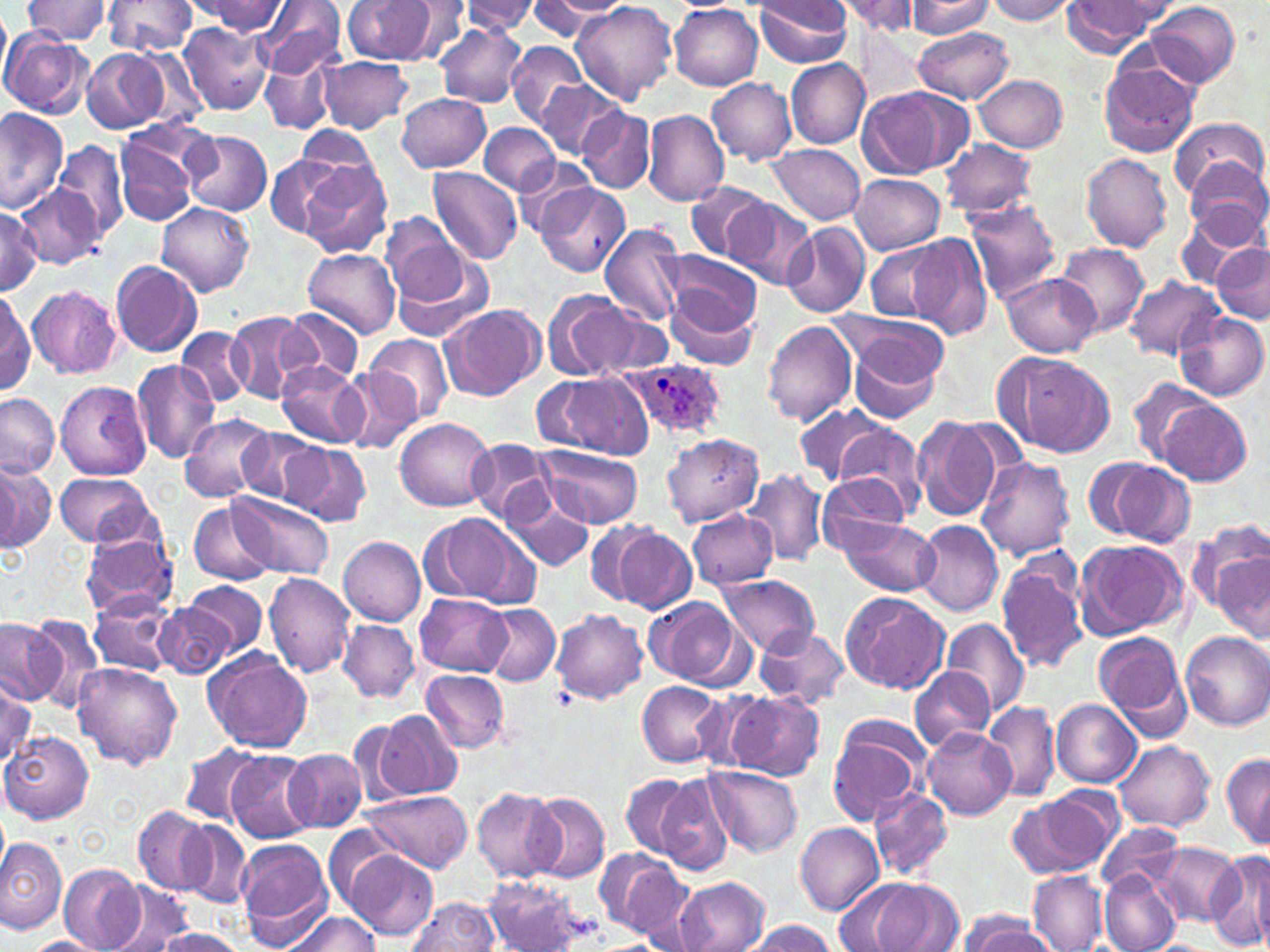

Summary:
  - Coordinate format: approximate bounding boxes as named x1/y1/x2/y2 corners in pixels
  - Plasmodium ovale-infected red blood cell locations: (x1=623, y1=358, x2=727, y2=441)
  - Uninfected red blood cell locations: (x1=23, y1=0, x2=113, y2=44), (x1=102, y1=0, x2=197, y2=57), (x1=256, y1=0, x2=345, y2=81), (x1=343, y1=0, x2=437, y2=64), (x1=752, y1=0, x2=854, y2=67), (x1=985, y1=0, x2=1077, y2=23), (x1=192, y1=1, x2=287, y2=35), (x1=402, y1=1, x2=472, y2=61), (x1=460, y1=1, x2=541, y2=34), (x1=538, y1=1, x2=629, y2=22), (x1=835, y1=1, x2=925, y2=35), (x1=905, y1=1, x2=996, y2=37), (x1=1061, y1=1, x2=1175, y2=54), (x1=529, y1=2, x2=616, y2=39), (x1=569, y1=2, x2=678, y2=107), (x1=1147, y1=2, x2=1241, y2=86), (x1=0, y1=6, x2=13, y2=89), (x1=670, y1=6, x2=763, y2=89), (x1=178, y1=23, x2=274, y2=115), (x1=435, y1=23, x2=526, y2=107), (x1=910, y1=27, x2=1015, y2=104), (x1=0, y1=31, x2=92, y2=118), (x1=506, y1=39, x2=587, y2=130), (x1=81, y1=47, x2=169, y2=132), (x1=260, y1=52, x2=339, y2=135), (x1=317, y1=56, x2=413, y2=134), (x1=1098, y1=56, x2=1200, y2=159), (x1=786, y1=57, x2=871, y2=149), (x1=776, y1=61, x2=879, y2=225), (x1=975, y1=75, x2=1069, y2=152), (x1=535, y1=78, x2=626, y2=160), (x1=707, y1=78, x2=797, y2=164), (x1=858, y1=87, x2=963, y2=178), (x1=398, y1=92, x2=491, y2=173), (x1=577, y1=107, x2=655, y2=193), (x1=0, y1=110, x2=68, y2=213), (x1=643, y1=110, x2=730, y2=207), (x1=1170, y1=117, x2=1266, y2=202), (x1=479, y1=121, x2=561, y2=196), (x1=294, y1=128, x2=383, y2=208), (x1=182, y1=130, x2=273, y2=215), (x1=940, y1=138, x2=1037, y2=220), (x1=113, y1=139, x2=197, y2=228), (x1=54, y1=140, x2=128, y2=239), (x1=766, y1=145, x2=865, y2=225), (x1=1080, y1=152, x2=1174, y2=251), (x1=264, y1=153, x2=349, y2=240), (x1=513, y1=155, x2=597, y2=237), (x1=1186, y1=157, x2=1269, y2=246), (x1=299, y1=161, x2=394, y2=260), (x1=427, y1=166, x2=523, y2=265), (x1=850, y1=176, x2=944, y2=254), (x1=534, y1=181, x2=629, y2=277), (x1=686, y1=182, x2=770, y2=260), (x1=20, y1=188, x2=99, y2=270), (x1=722, y1=196, x2=817, y2=289), (x1=962, y1=198, x2=1061, y2=302), (x1=156, y1=201, x2=255, y2=297), (x1=0, y1=204, x2=43, y2=293), (x1=1175, y1=204, x2=1265, y2=287), (x1=381, y1=214, x2=470, y2=307), (x1=599, y1=222, x2=688, y2=329), (x1=781, y1=222, x2=871, y2=319), (x1=906, y1=232, x2=993, y2=339), (x1=863, y1=241, x2=955, y2=323), (x1=1210, y1=242, x2=1270, y2=322), (x1=1057, y1=243, x2=1150, y2=336), (x1=389, y1=247, x2=496, y2=343), (x1=302, y1=248, x2=400, y2=339), (x1=667, y1=251, x2=764, y2=332), (x1=110, y1=260, x2=202, y2=357), (x1=999, y1=273, x2=1100, y2=356), (x1=1124, y1=274, x2=1223, y2=358), (x1=27, y1=284, x2=122, y2=378), (x1=663, y1=288, x2=759, y2=371), (x1=1, y1=290, x2=35, y2=393), (x1=542, y1=290, x2=638, y2=383), (x1=440, y1=304, x2=544, y2=400), (x1=585, y1=305, x2=676, y2=380), (x1=283, y1=308, x2=363, y2=386), (x1=225, y1=311, x2=315, y2=403), (x1=1173, y1=311, x2=1267, y2=402), (x1=838, y1=314, x2=949, y2=417), (x1=762, y1=319, x2=858, y2=427), (x1=175, y1=327, x2=254, y2=407), (x1=364, y1=333, x2=453, y2=424), (x1=999, y1=350, x2=1115, y2=458), (x1=131, y1=360, x2=222, y2=464), (x1=277, y1=360, x2=369, y2=450), (x1=340, y1=371, x2=422, y2=451), (x1=541, y1=373, x2=653, y2=459), (x1=55, y1=380, x2=150, y2=480), (x1=1128, y1=380, x2=1219, y2=466), (x1=0, y1=393, x2=59, y2=479), (x1=1157, y1=399, x2=1252, y2=485), (x1=795, y1=403, x2=891, y2=487), (x1=180, y1=412, x2=275, y2=502), (x1=910, y1=415, x2=1004, y2=524), (x1=395, y1=417, x2=495, y2=512), (x1=834, y1=425, x2=929, y2=520), (x1=235, y1=427, x2=320, y2=503), (x1=663, y1=433, x2=765, y2=525), (x1=465, y1=439, x2=555, y2=523), (x1=280, y1=442, x2=371, y2=527), (x1=537, y1=446, x2=643, y2=527), (x1=976, y1=456, x2=1076, y2=561), (x1=1083, y1=457, x2=1194, y2=547), (x1=0, y1=460, x2=52, y2=552), (x1=742, y1=470, x2=829, y2=567), (x1=55, y1=474, x2=152, y2=548), (x1=818, y1=474, x2=911, y2=556), (x1=502, y1=482, x2=596, y2=574), (x1=230, y1=492, x2=333, y2=579), (x1=189, y1=500, x2=275, y2=586), (x1=688, y1=510, x2=778, y2=590), (x1=424, y1=512, x2=538, y2=611), (x1=837, y1=517, x2=939, y2=597), (x1=1186, y1=519, x2=1270, y2=617), (x1=586, y1=520, x2=666, y2=607), (x1=913, y1=520, x2=1003, y2=615), (x1=612, y1=528, x2=698, y2=613), (x1=80, y1=531, x2=180, y2=617), (x1=339, y1=537, x2=427, y2=625), (x1=1075, y1=539, x2=1187, y2=639), (x1=1212, y1=550, x2=1270, y2=638), (x1=995, y1=552, x2=1089, y2=673), (x1=264, y1=572, x2=354, y2=677), (x1=717, y1=573, x2=821, y2=656), (x1=187, y1=579, x2=268, y2=656), (x1=840, y1=590, x2=951, y2=695), (x1=90, y1=594, x2=178, y2=677), (x1=416, y1=595, x2=511, y2=676), (x1=644, y1=596, x2=746, y2=688), (x1=155, y1=600, x2=235, y2=679), (x1=478, y1=603, x2=559, y2=686), (x1=551, y1=608, x2=648, y2=704), (x1=26, y1=614, x2=107, y2=711), (x1=939, y1=616, x2=1031, y2=719), (x1=0, y1=618, x2=63, y2=704), (x1=338, y1=620, x2=418, y2=703), (x1=754, y1=625, x2=850, y2=709), (x1=1092, y1=631, x2=1191, y2=735), (x1=1181, y1=631, x2=1270, y2=730), (x1=204, y1=650, x2=314, y2=753), (x1=74, y1=664, x2=183, y2=769), (x1=911, y1=665, x2=994, y2=753), (x1=422, y1=668, x2=510, y2=753), (x1=1, y1=675, x2=36, y2=765), (x1=637, y1=681, x2=725, y2=767), (x1=724, y1=691, x2=825, y2=781), (x1=1052, y1=700, x2=1142, y2=787), (x1=983, y1=701, x2=1061, y2=802), (x1=372, y1=709, x2=464, y2=799), (x1=826, y1=714, x2=931, y2=826), (x1=920, y1=727, x2=1016, y2=819), (x1=2, y1=732, x2=92, y2=824), (x1=1114, y1=741, x2=1215, y2=831), (x1=180, y1=744, x2=261, y2=825), (x1=283, y1=749, x2=369, y2=834), (x1=225, y1=750, x2=319, y2=843), (x1=1220, y1=754, x2=1270, y2=850), (x1=706, y1=766, x2=802, y2=858), (x1=620, y1=773, x2=697, y2=859), (x1=655, y1=774, x2=735, y2=875), (x1=472, y1=787, x2=561, y2=880), (x1=1014, y1=788, x2=1123, y2=877), (x1=868, y1=789, x2=954, y2=883), (x1=363, y1=791, x2=473, y2=873), (x1=527, y1=791, x2=610, y2=883), (x1=134, y1=806, x2=214, y2=894), (x1=179, y1=820, x2=253, y2=909), (x1=794, y1=822, x2=884, y2=914), (x1=1096, y1=824, x2=1185, y2=893), (x1=0, y1=837, x2=67, y2=933), (x1=235, y1=839, x2=333, y2=947), (x1=1150, y1=844, x2=1240, y2=926), (x1=341, y1=848, x2=438, y2=942), (x1=595, y1=849, x2=690, y2=941), (x1=1207, y1=851, x2=1270, y2=952), (x1=58, y1=864, x2=144, y2=952), (x1=1099, y1=869, x2=1182, y2=952), (x1=1029, y1=872, x2=1108, y2=951), (x1=484, y1=877, x2=586, y2=950), (x1=673, y1=877, x2=772, y2=952), (x1=839, y1=877, x2=964, y2=952), (x1=107, y1=883, x2=197, y2=952), (x1=406, y1=897, x2=499, y2=952), (x1=281, y1=911, x2=382, y2=952), (x1=961, y1=915, x2=1057, y2=952), (x1=741, y1=919, x2=837, y2=952), (x1=153, y1=927, x2=246, y2=952), (x1=25, y1=935, x2=105, y2=952)
  - Slide-level diagnosis: Plasmodium ovale
  - Preparation: thin blood film
  - Magnification: 1000x
  - Field of view: single
  - Stain: May-Grünwald-Giemsa
  - Modality: optical microscopy
  - Image size: 1270×952 pixels